Assess for malaria.
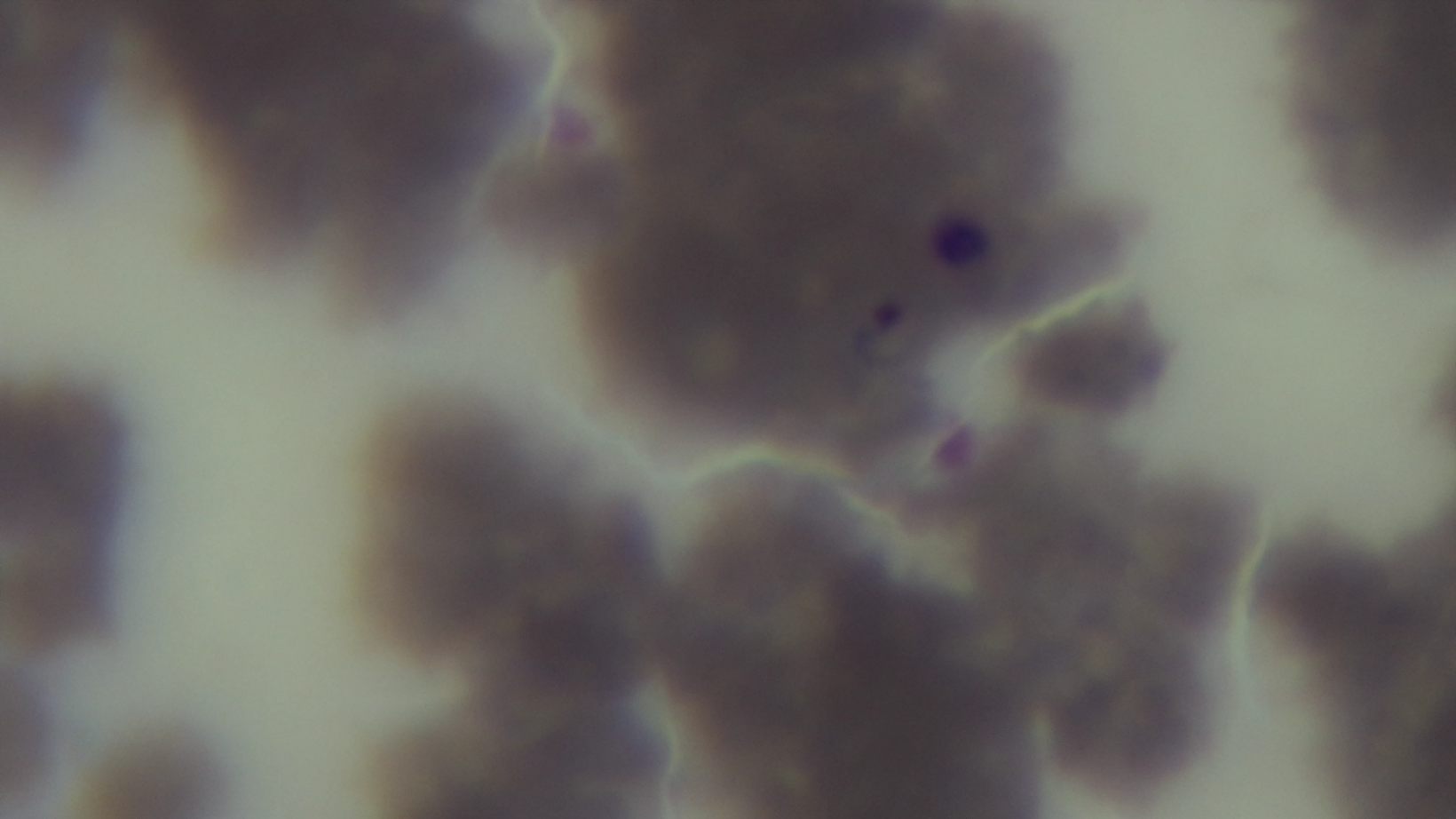
Infected.

modality: light microscopy
capture: mounted 4K digital camera
objective: 100x oil immersion
field_of_view: single
preparation: thin blood film
stain: Giemsa